Classify this cell by malaria status.
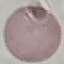

It is uninfected.

preparation = thin blood film
image type = cell patch, automatically extracted from a larger field of view and resized to 64 × 64 pixels
stain = Giemsa
capture = smartphone camera at the microscope eyepiece